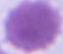

modality = photomicrograph
magnification = 1000x
identification = red blood cell